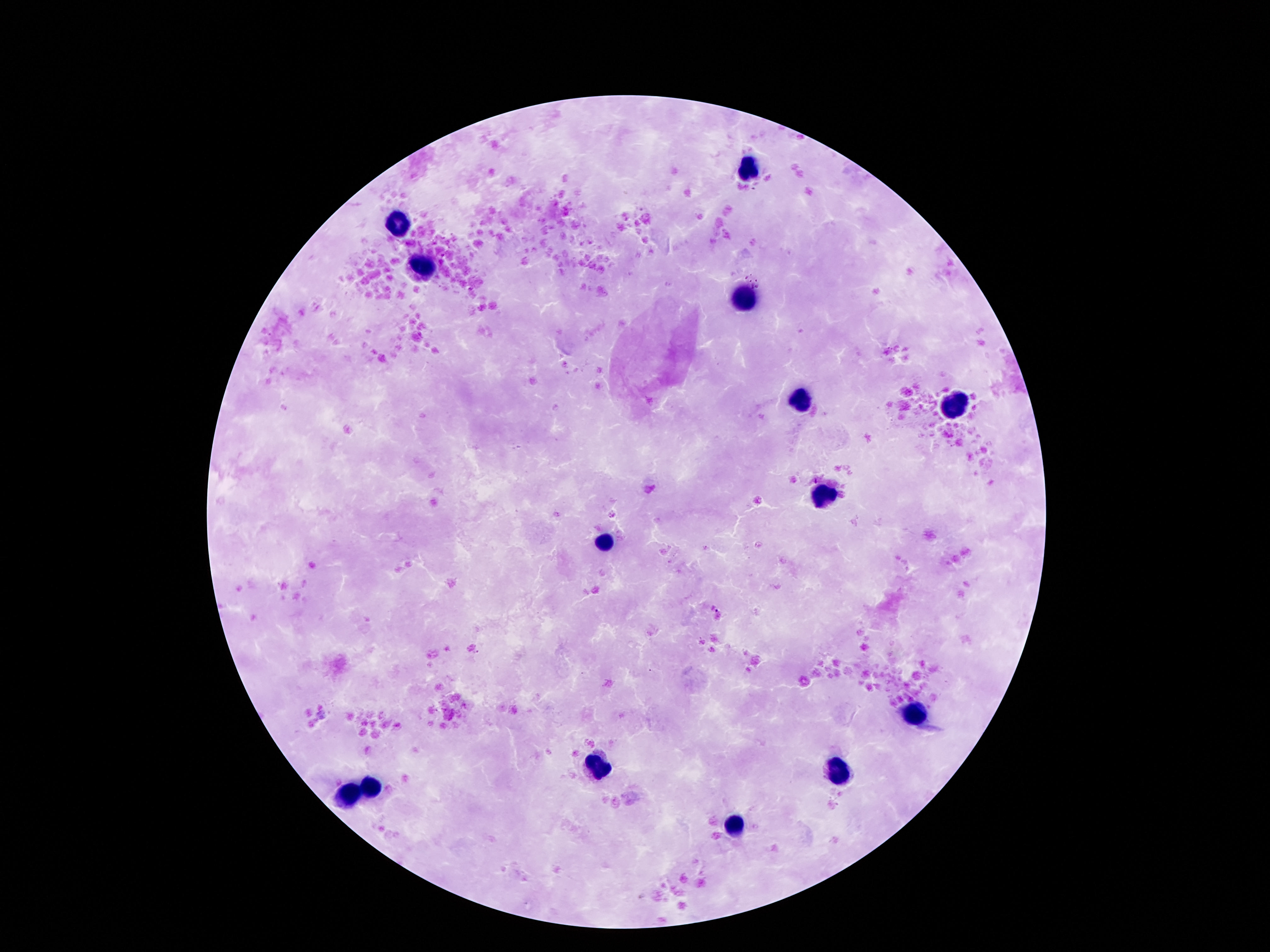 Approximate object centers, in pixels from the top-left corner. Leukocyte locations: (x=747, y=170), (x=401, y=224), (x=425, y=266), (x=743, y=299), (x=801, y=401), (x=955, y=405), (x=822, y=496), (x=602, y=543), (x=918, y=715), (x=599, y=766), (x=836, y=772), (x=372, y=783), (x=352, y=794), (x=736, y=827). Giemsa stain. Thick peripheral-blood smear. Image is 1270×952 pixels. 100x magnification. One field from this slide. Patient malaria status: negative. Photographed through the microscope eyepiece with a smartphone camera.